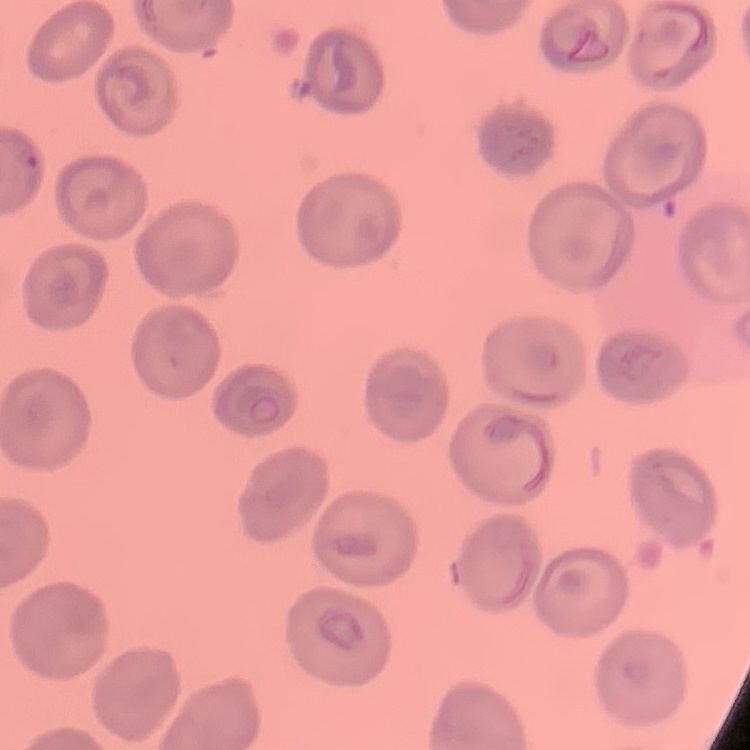

The erythrocytes exhibit no rouleaux formation. Square crop of a larger photomicrograph. Thin blood smear. Stained with either Field's or Giemsa.